Assess this cell for malaria.
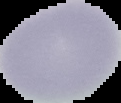
It is uninfected.

Summary:
  - Preparation: thin blood smear
  - Image type: cell region segmented out of the field of view; surrounding area masked to black
  - Image size: 121×103 pixels